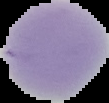
The area outside the segmented cell region is set to black. Image is 109×103 pixels. From a thin blood smear. Result: no Plasmodium parasites seen.